Outline each Plasmodium ovale-infected red blood cell.
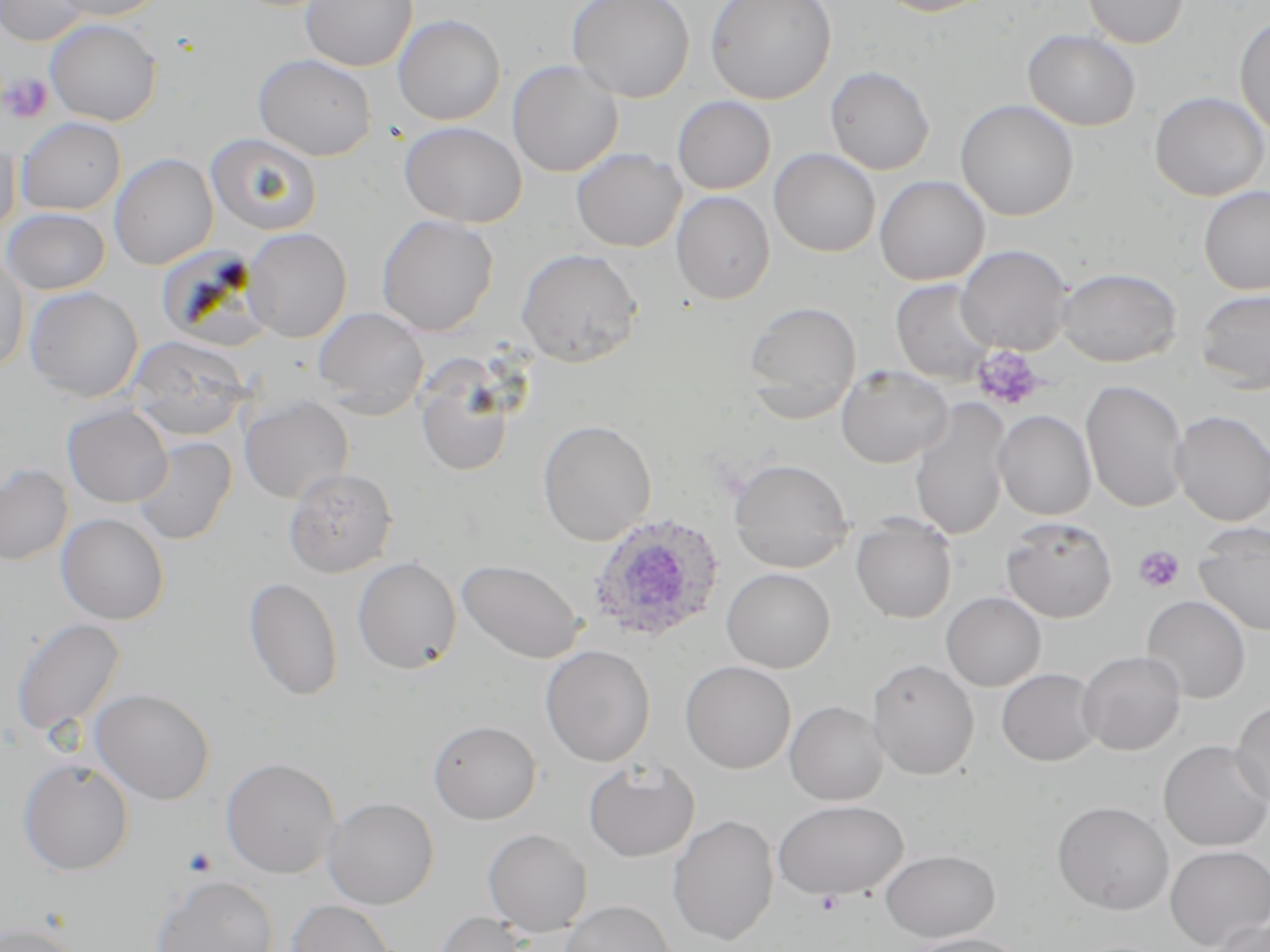
Approximate bounding boxes as [x1, y1, x2, y2] in pixels.
Plasmodium ovale-infected red blood cells: [587, 513, 727, 643].

Summary:
  - Platelet locations: [2, 73, 52, 122], [972, 345, 1045, 412], [1134, 546, 1184, 593], [181, 846, 218, 877], [813, 889, 844, 914]
  - Uninfected red blood cell locations: [1, 0, 92, 46], [49, 0, 166, 21], [301, 0, 417, 72], [567, 0, 695, 102], [705, 0, 837, 104], [872, 0, 996, 17], [1082, 0, 1189, 48], [393, 15, 505, 126], [1234, 15, 1270, 139], [45, 18, 162, 126], [1023, 29, 1141, 131], [254, 54, 376, 161], [507, 60, 623, 177], [824, 65, 934, 175], [1149, 91, 1269, 201], [672, 96, 775, 194], [955, 99, 1079, 221], [15, 117, 126, 215], [399, 121, 527, 227], [0, 132, 21, 238], [206, 133, 322, 236], [571, 147, 686, 252], [769, 148, 880, 257], [109, 153, 218, 270], [874, 175, 989, 285], [1199, 186, 1270, 295], [671, 191, 775, 304], [1, 208, 111, 294], [376, 214, 499, 336], [243, 228, 352, 342], [956, 244, 1073, 355], [516, 247, 644, 367], [0, 251, 30, 375], [1057, 267, 1182, 366], [891, 279, 997, 385], [25, 286, 144, 402], [1195, 287, 1270, 394], [743, 300, 861, 419], [313, 307, 429, 419], [127, 334, 252, 442], [414, 358, 516, 478], [836, 365, 954, 468], [1080, 379, 1190, 513], [239, 395, 354, 503], [909, 399, 1012, 541], [62, 405, 172, 508], [994, 409, 1096, 520], [1172, 410, 1270, 527], [538, 419, 657, 545], [132, 437, 237, 545], [728, 458, 854, 571], [0, 463, 73, 566], [284, 466, 398, 577], [56, 513, 170, 625], [851, 516, 956, 623], [1000, 516, 1117, 623], [1193, 523, 1270, 636], [353, 556, 462, 674], [457, 559, 583, 663], [722, 568, 835, 673], [244, 576, 343, 700], [941, 591, 1046, 692], [1141, 595, 1251, 704], [11, 617, 125, 738], [540, 645, 656, 767], [1077, 649, 1186, 755], [866, 657, 979, 779], [680, 660, 796, 773], [996, 668, 1102, 767], [90, 688, 215, 804], [1231, 699, 1270, 808], [785, 700, 889, 805], [429, 719, 541, 824], [1158, 740, 1270, 851], [221, 758, 341, 878], [18, 759, 135, 875], [583, 759, 701, 862], [323, 797, 439, 909], [772, 799, 908, 900], [1052, 800, 1174, 915], [667, 814, 779, 945], [483, 828, 592, 937], [1165, 844, 1270, 950], [880, 849, 999, 941], [151, 875, 278, 952], [286, 900, 396, 952], [560, 900, 677, 952], [433, 911, 534, 952], [1207, 916, 1270, 952], [1, 922, 86, 952], [901, 932, 1031, 952]
  - Slide-level diagnosis: Plasmodium ovale
  - Modality: optical microscopy
  - Preparation: thin blood film
  - Magnification: 1000x
  - Image size: 1270×952 pixels
  - Stain: May-Grünwald-Giemsa
  - Field of view: one of a larger specimen